State which parasite is depicted.
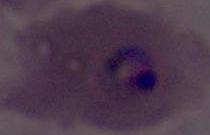

This is Plasmodium.

Summary:
  - Modality: micrograph
  - Magnification: 400x or 1000x